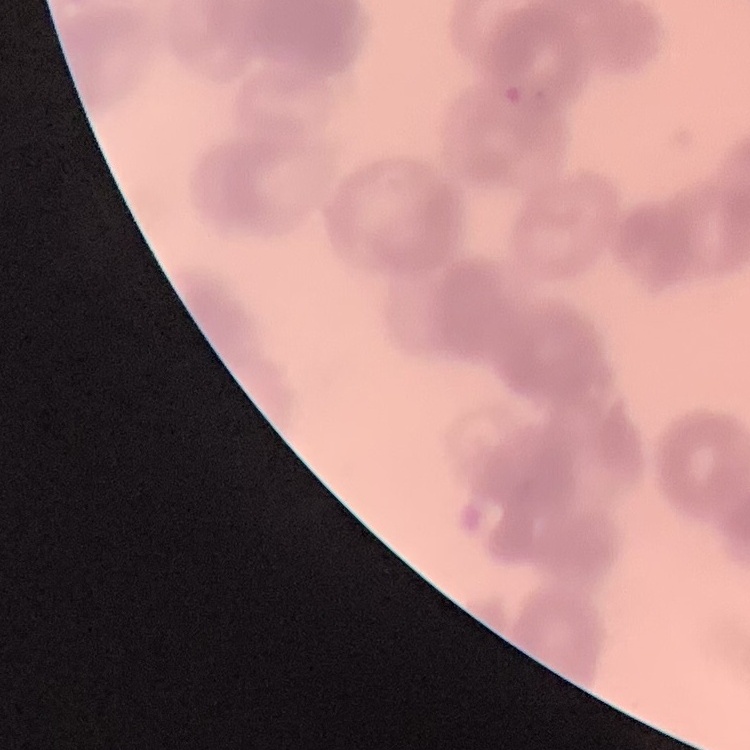 The red blood cells exhibit rouleaux formation. Field's or Giemsa stain. Thin blood smear. One tile cut from a larger photomicrograph.